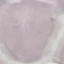

malaria_status: uninfected
capture: smartphone camera at the microscope eyepiece
preparation: thin smear
image_type: automatically extracted cell patch, resized to 64 × 64 pixels
stain: Giemsa